Give the position of every leukocyte visible.
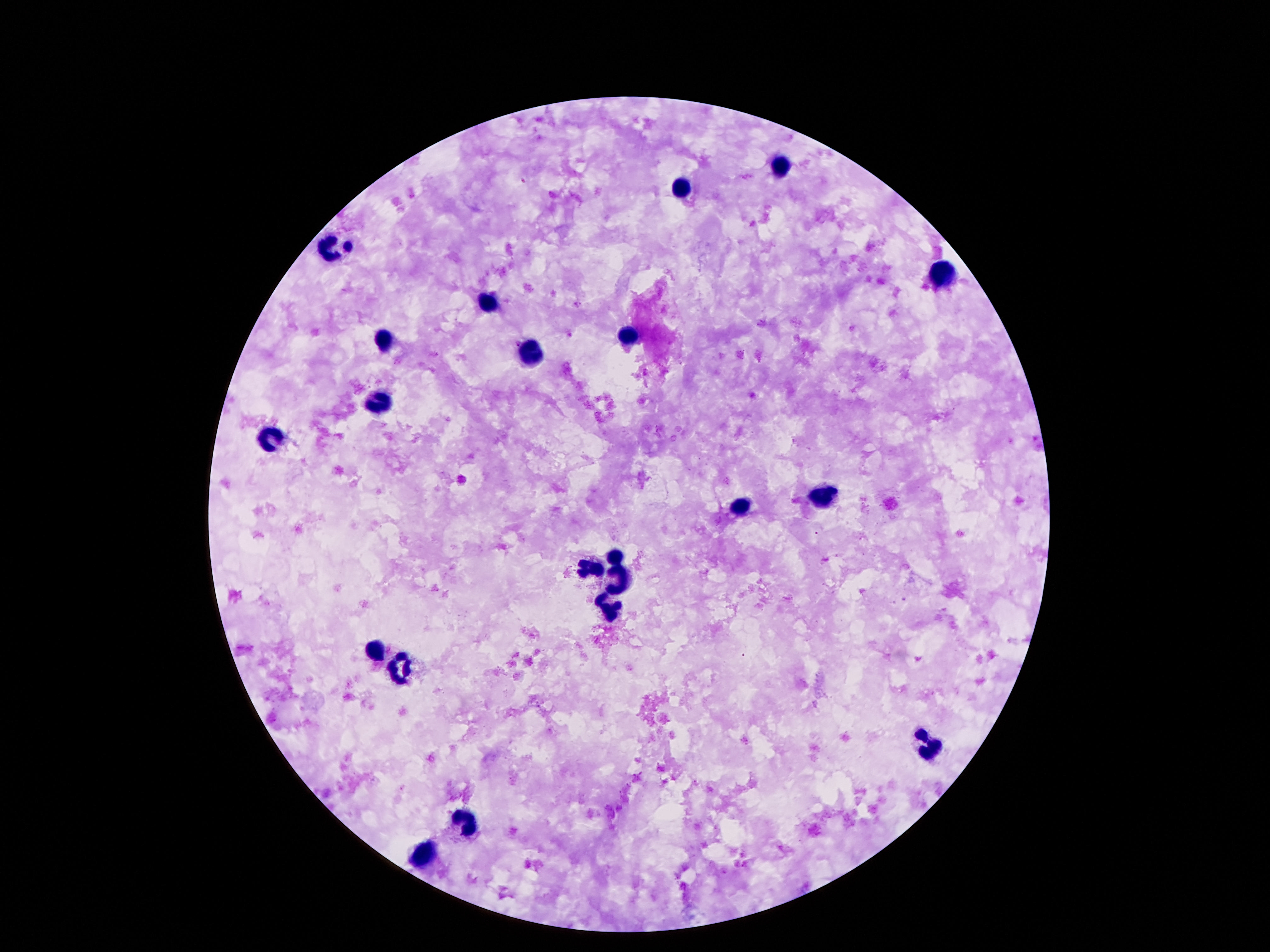

Approximate centers as [x, y] in pixels.
Leukocytes: [780, 167], [679, 188], [335, 248], [940, 274], [487, 304], [384, 337], [628, 338], [533, 351], [380, 401], [276, 438], [823, 494], [740, 506], [613, 553], [587, 568], [621, 580], [604, 608], [375, 652], [399, 667], [929, 744], [466, 820], [425, 856].

patient malaria status = uninfected
image size = 1270×952 pixels
preparation = thick blood smear
capture = smartphone camera through the microscope eyepiece
stain = Giemsa
magnification = 100x
field of view = single